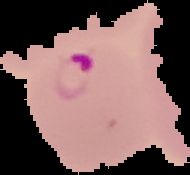
preparation = thin blood smear
result = Plasmodium parasites detected
image type = cell region segmented out of the field of view; surrounding area masked to black
image size = 190×175 pixels